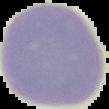

image type = cell region segmented out of the field of view; surrounding area masked to black
preparation = thin blood film
malaria status = uninfected
image size = 109×109 pixels